Outline each blood parasite and name the species.
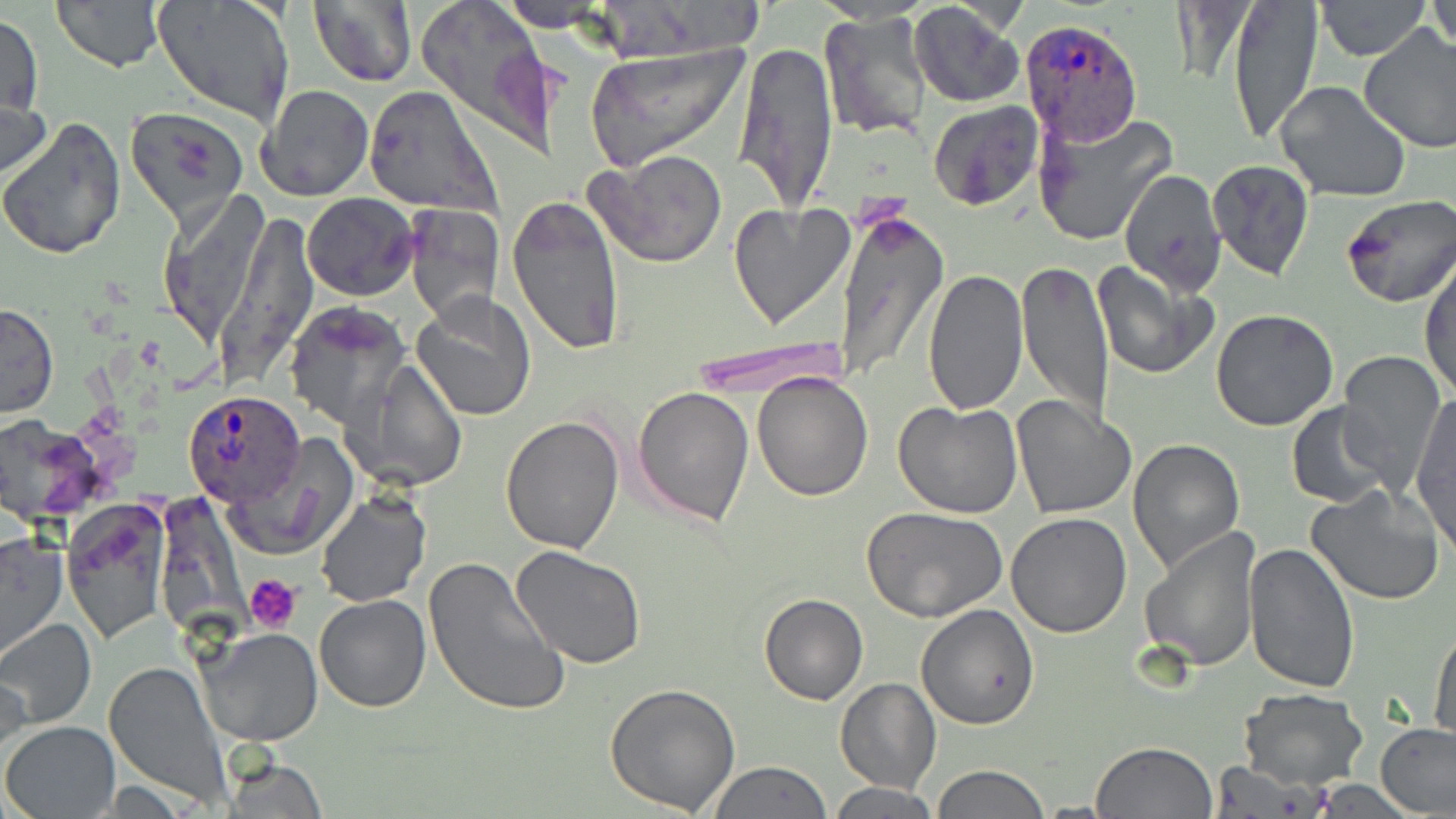
Approximate bounding boxes as named x1/y1/x2/y2 corners in pixels.
Plasmodium ovale-infected red blood cells: (x1=1020, y1=17, x2=1144, y2=144), (x1=181, y1=391, x2=310, y2=510).
No Plasmodium falciparum, Plasmodium malariae, Plasmodium vivax, Babesia divergens, or Trypanosoma brucei observed.

Summary:
  - Uninfected red blood cell locations: (x1=50, y1=0, x2=167, y2=73), (x1=151, y1=0, x2=296, y2=127), (x1=309, y1=0, x2=416, y2=88), (x1=413, y1=0, x2=560, y2=155), (x1=1226, y1=0, x2=1322, y2=144), (x1=1314, y1=0, x2=1432, y2=62), (x1=499, y1=1, x2=602, y2=25), (x1=908, y1=1, x2=1024, y2=107), (x1=1429, y1=1, x2=1455, y2=59), (x1=1, y1=11, x2=43, y2=120), (x1=818, y1=11, x2=935, y2=142), (x1=1359, y1=25, x2=1456, y2=153), (x1=734, y1=39, x2=839, y2=214), (x1=583, y1=42, x2=749, y2=172), (x1=0, y1=80, x2=52, y2=197), (x1=1275, y1=81, x2=1413, y2=204), (x1=258, y1=84, x2=375, y2=201), (x1=365, y1=86, x2=500, y2=215), (x1=927, y1=100, x2=1043, y2=211), (x1=128, y1=107, x2=251, y2=231), (x1=1034, y1=109, x2=1179, y2=245), (x1=0, y1=118, x2=127, y2=259), (x1=587, y1=149, x2=729, y2=269), (x1=1208, y1=160, x2=1314, y2=281), (x1=1119, y1=170, x2=1226, y2=293), (x1=159, y1=191, x2=268, y2=352), (x1=302, y1=193, x2=418, y2=301), (x1=506, y1=194, x2=627, y2=356), (x1=1338, y1=195, x2=1456, y2=308), (x1=729, y1=201, x2=855, y2=330), (x1=404, y1=203, x2=501, y2=325), (x1=833, y1=208, x2=947, y2=385), (x1=1421, y1=254, x2=1456, y2=399), (x1=1017, y1=259, x2=1112, y2=432), (x1=1092, y1=261, x2=1218, y2=380), (x1=921, y1=268, x2=1029, y2=418), (x1=411, y1=299, x2=508, y2=422), (x1=284, y1=301, x2=410, y2=427), (x1=0, y1=302, x2=59, y2=419), (x1=1209, y1=309, x2=1340, y2=431), (x1=688, y1=336, x2=854, y2=397), (x1=1337, y1=351, x2=1446, y2=488), (x1=346, y1=359, x2=467, y2=492), (x1=753, y1=373, x2=873, y2=501), (x1=632, y1=385, x2=755, y2=526), (x1=1412, y1=394, x2=1455, y2=550), (x1=1009, y1=395, x2=1130, y2=519), (x1=894, y1=399, x2=1023, y2=518), (x1=1286, y1=402, x2=1395, y2=508), (x1=501, y1=415, x2=624, y2=554), (x1=228, y1=438, x2=355, y2=560), (x1=1128, y1=438, x2=1246, y2=578), (x1=1305, y1=483, x2=1447, y2=605), (x1=315, y1=491, x2=430, y2=607), (x1=60, y1=500, x2=171, y2=643), (x1=863, y1=508, x2=1007, y2=622), (x1=1005, y1=513, x2=1132, y2=637), (x1=1139, y1=526, x2=1259, y2=672), (x1=0, y1=530, x2=69, y2=663), (x1=1244, y1=542, x2=1361, y2=694), (x1=510, y1=546, x2=646, y2=668), (x1=422, y1=556, x2=569, y2=717), (x1=759, y1=593, x2=868, y2=705), (x1=314, y1=594, x2=431, y2=712), (x1=915, y1=604, x2=1039, y2=730), (x1=0, y1=618, x2=98, y2=731), (x1=1429, y1=620, x2=1456, y2=743), (x1=195, y1=627, x2=323, y2=746), (x1=104, y1=659, x2=231, y2=807), (x1=0, y1=664, x2=30, y2=767), (x1=835, y1=678, x2=940, y2=795), (x1=605, y1=681, x2=740, y2=816), (x1=1238, y1=688, x2=1367, y2=790), (x1=2, y1=721, x2=120, y2=817), (x1=1376, y1=721, x2=1456, y2=817), (x1=1092, y1=741, x2=1218, y2=818), (x1=218, y1=750, x2=329, y2=819), (x1=709, y1=760, x2=833, y2=818), (x1=1210, y1=763, x2=1326, y2=817), (x1=930, y1=765, x2=1051, y2=819), (x1=829, y1=782, x2=940, y2=818)
  - Platelet locations: (x1=245, y1=573, x2=305, y2=633)
  - Slide-level diagnosis: Plasmodium ovale
  - Magnification: 1000x
  - Field of view: one of a larger specimen
  - Preparation: thin blood film
  - Image size: 1456×819 pixels
  - Stain: May-Grünwald-Giemsa
  - Modality: optical microscopy